Assess this cell for malaria.
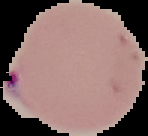
Parasitized.

Image is 148×136 pixels. From a thin blood smear. Cell region segmented out of the field of view; the surrounding area is masked to black.